Comment on the morphology of the erythrocytes.
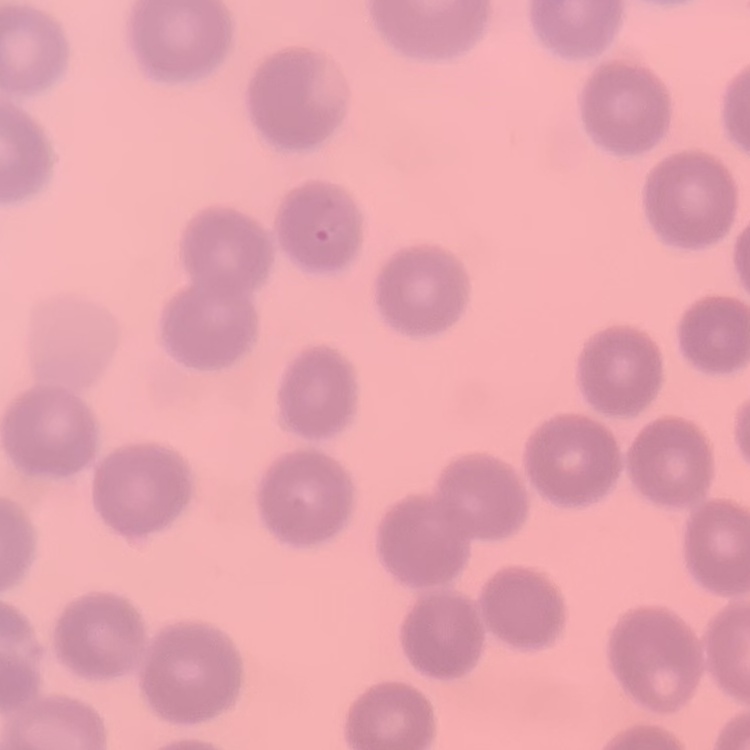

No rouleaux formation.

preparation: thin blood film
stain: Field's or Giemsa
image_type: one tile cut from a larger photomicrograph